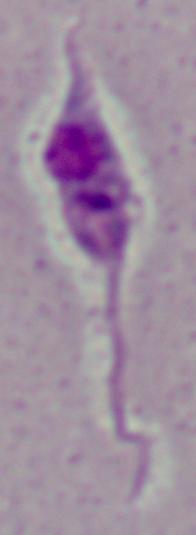
Photomicrograph. 1000x magnification. A Leishmania parasite is seen.